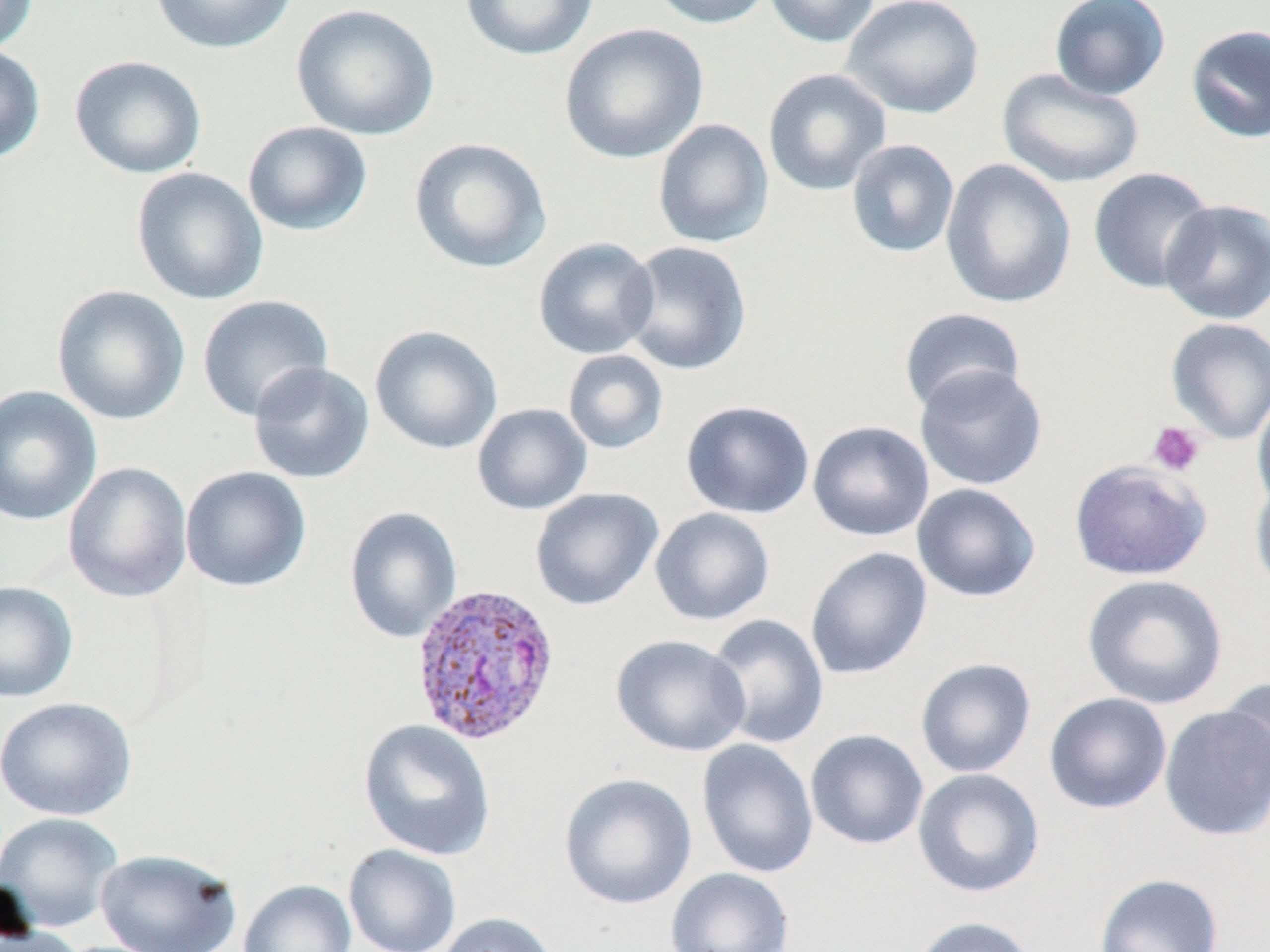

Approximate bounding boxes as (x1,y1)-(x2,y2) corner pairs in pixels. Platelet locations: (1147,421)-(1206,476). Uninfected red blood cell locations: (0,0)-(40,54), (149,0)-(298,54), (460,0)-(598,61), (649,0)-(773,29), (763,0)-(881,48), (841,0)-(984,119), (1049,0)-(1171,101), (290,3)-(440,141), (559,23)-(708,163), (1184,23)-(1270,143), (0,45)-(47,164), (69,55)-(207,179), (762,68)-(892,197), (997,68)-(1145,189), (652,118)-(774,248), (241,120)-(374,237), (408,138)-(552,274), (845,139)-(960,259), (940,158)-(1076,310), (131,166)-(268,305), (1088,167)-(1217,294), (1159,199)-(1270,325), (533,238)-(660,359), (620,240)-(752,376), (51,285)-(190,425), (197,295)-(334,422), (898,307)-(1027,415), (1165,317)-(1270,445), (369,326)-(502,455), (563,349)-(668,454), (248,361)-(375,484), (914,365)-(1048,492), (0,385)-(102,526), (1252,390)-(1270,516), (680,399)-(816,519), (472,402)-(593,515), (807,420)-(935,541), (1068,459)-(1212,581), (63,461)-(192,603), (180,466)-(312,593), (1249,475)-(1270,598), (911,483)-(1041,602), (530,488)-(663,611), (344,506)-(462,643), (650,507)-(776,626), (805,547)-(933,681), (1081,574)-(1229,710), (0,580)-(79,703), (705,614)-(829,749), (611,634)-(751,757), (915,657)-(1037,778), (1220,676)-(1270,799), (1044,692)-(1172,814), (1,697)-(136,821), (1159,705)-(1270,841), (358,719)-(496,861), (804,729)-(929,850), (697,738)-(819,879), (913,768)-(1045,897), (558,773)-(698,910), (0,812)-(123,932), (343,844)-(461,952), (94,848)-(242,951), (666,866)-(795,952), (1094,872)-(1224,952), (238,879)-(357,952), (435,912)-(559,952), (910,916)-(1039,952). Plasmodium vivax-infected red blood cell locations: (409,583)-(562,746). Slide-level diagnosis: Plasmodium vivax. Light microscopy. 1000x magnification. Image is 1270×952 pixels. Thin blood film. Single field of view. May-Grünwald-Giemsa stain.